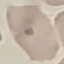
Summary:
  - Malaria status: uninfected
  - Image type: automatically extracted cell patch, resized to 64 × 64 pixels
  - Capture: smartphone through the microscope eyepiece
  - Stain: Giemsa
  - Preparation: thin smear